Identify the parasite.
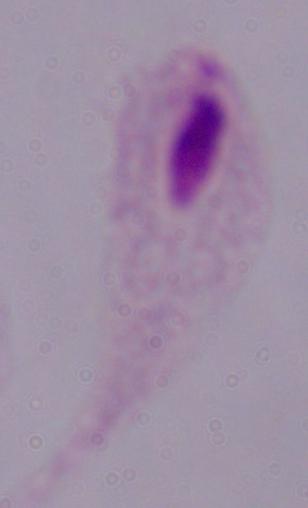

A trichomonad.

1000x magnification. Photomicrograph.